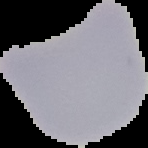

Segmented cell region on a black background. Malaria status: uninfected. From a thin blood film. Image is 148×148 pixels.